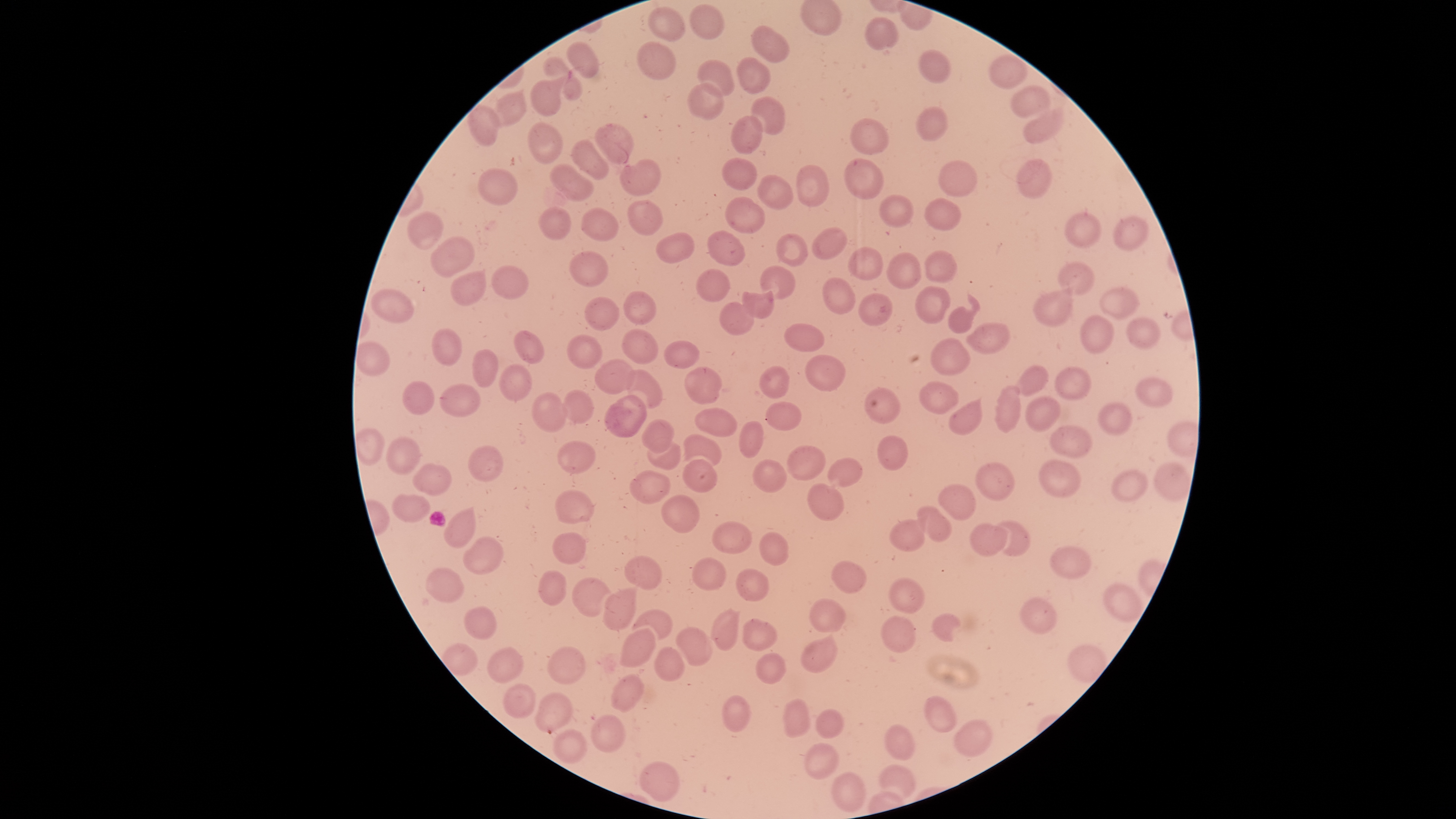 Approximate bounding boxes as (left, top, right, bottom) in pixels. Parasitized RBCs: (535, 693, 574, 734). Uninfected RBCs: (691, 4, 724, 40), (649, 8, 686, 41), (866, 17, 899, 51), (752, 26, 789, 64), (568, 42, 598, 79), (639, 42, 675, 81), (919, 51, 951, 83), (989, 55, 1027, 89), (545, 56, 581, 101), (738, 57, 770, 94), (699, 59, 734, 97), (531, 79, 560, 117), (686, 83, 725, 120), (1009, 86, 1051, 120), (491, 91, 526, 128), (751, 97, 785, 137), (469, 105, 500, 146), (916, 107, 948, 142), (1022, 110, 1066, 144), (729, 116, 765, 153), (850, 118, 889, 154), (528, 122, 562, 166), (595, 124, 633, 164), (572, 138, 609, 180), (721, 157, 758, 191), (843, 158, 884, 198), (621, 159, 660, 196), (939, 160, 978, 196), (1016, 160, 1052, 198), (551, 163, 594, 202), (797, 165, 830, 206), (479, 167, 518, 206), (757, 174, 794, 210), (880, 195, 914, 228), (725, 197, 765, 235), (923, 198, 960, 232), (628, 201, 663, 236), (538, 207, 571, 240), (582, 207, 618, 242), (407, 210, 444, 250), (1065, 213, 1101, 248), (1113, 216, 1149, 252), (812, 228, 846, 259), (707, 232, 746, 265), (655, 233, 695, 264), (775, 233, 808, 267), (430, 236, 475, 276), (848, 246, 884, 281), (570, 251, 608, 288), (922, 251, 959, 283), (885, 252, 922, 291), (1057, 264, 1095, 295), (491, 266, 530, 299), (760, 266, 795, 299), (696, 270, 730, 303), (449, 271, 488, 307), (823, 277, 856, 314), (743, 282, 773, 320), (915, 284, 952, 324), (370, 288, 414, 323), (1100, 288, 1140, 318), (1033, 289, 1074, 328), (624, 292, 657, 324), (858, 292, 893, 327), (586, 297, 618, 333), (720, 300, 753, 337), (947, 307, 975, 334), (1080, 316, 1114, 354), (1125, 317, 1162, 348), (968, 322, 1011, 354), (784, 323, 825, 352), (433, 328, 462, 365), (515, 329, 545, 365), (623, 330, 658, 365), (568, 335, 603, 369), (930, 336, 971, 375), (664, 341, 700, 369), (472, 348, 498, 389), (804, 356, 846, 391), (594, 358, 637, 395), (500, 363, 532, 402), (758, 366, 791, 398), (1018, 366, 1048, 397), (1055, 367, 1091, 400), (684, 368, 722, 404), (627, 369, 663, 410), (1136, 375, 1173, 409), (400, 381, 435, 415), (918, 382, 960, 413), (439, 385, 480, 415), (996, 387, 1022, 432), (863, 388, 903, 422), (561, 390, 594, 422), (533, 394, 568, 432), (603, 395, 647, 436), (1025, 397, 1061, 431), (765, 400, 803, 432), (948, 400, 985, 437), (1099, 403, 1132, 435), (694, 408, 737, 436), (642, 420, 674, 454), (739, 420, 764, 458), (1050, 425, 1092, 457), (684, 434, 722, 469), (878, 435, 909, 472), (386, 437, 420, 474), (648, 437, 681, 471), (558, 441, 596, 473), (468, 445, 503, 482), (787, 445, 826, 480), (828, 458, 863, 488), (682, 459, 717, 493), (753, 459, 787, 493), (1039, 460, 1082, 496), (977, 461, 1014, 501), (1155, 461, 1191, 501), (413, 462, 452, 496), (1111, 469, 1149, 501), (630, 471, 670, 505), (807, 483, 845, 521), (939, 485, 976, 520), (556, 490, 594, 525), (391, 494, 430, 523), (659, 495, 700, 534), (916, 505, 952, 542), (443, 509, 477, 548), (890, 520, 926, 552), (993, 521, 1032, 556), (712, 522, 752, 554), (970, 524, 1010, 557), (553, 532, 585, 564), (760, 532, 788, 564), (464, 536, 505, 574), (1052, 546, 1091, 580), (625, 556, 662, 590), (692, 558, 726, 591), (829, 560, 868, 592), (425, 567, 464, 602), (539, 569, 568, 605), (736, 569, 769, 602), (573, 576, 610, 618), (889, 579, 925, 613), (1104, 583, 1144, 622), (603, 588, 637, 631), (809, 598, 847, 633), (1019, 598, 1056, 635), (463, 605, 498, 639), (711, 608, 739, 650), (632, 611, 672, 642), (932, 614, 962, 642), (882, 615, 917, 653), (742, 618, 778, 650), (676, 626, 712, 666), (617, 628, 657, 667), (801, 637, 839, 674), (487, 645, 524, 683), (654, 647, 686, 682), (547, 648, 584, 685), (756, 653, 786, 684), (613, 675, 642, 714), (503, 683, 536, 719), (722, 695, 750, 731), (923, 696, 957, 733), (783, 698, 810, 738), (815, 709, 843, 739), (591, 715, 625, 752), (955, 719, 991, 758), (883, 724, 915, 761), (553, 729, 587, 764), (805, 742, 839, 779), (640, 761, 678, 801), (879, 764, 915, 799), (832, 773, 866, 813). Species: Plasmodium falciparum. Photographed with a smartphone camera through the microscope eyepiece. Giemsa stain. Single field of view. Thin smear of blood. Image is 1456×819 pixels. The visible region is circular. Presence: malaria parasites detected.